Report the malaria status of this cell.
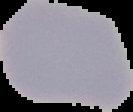

It is uninfected.

image size = 133×112 pixels
preparation = thin blood film
image type = segmented cell region with the area outside set to black